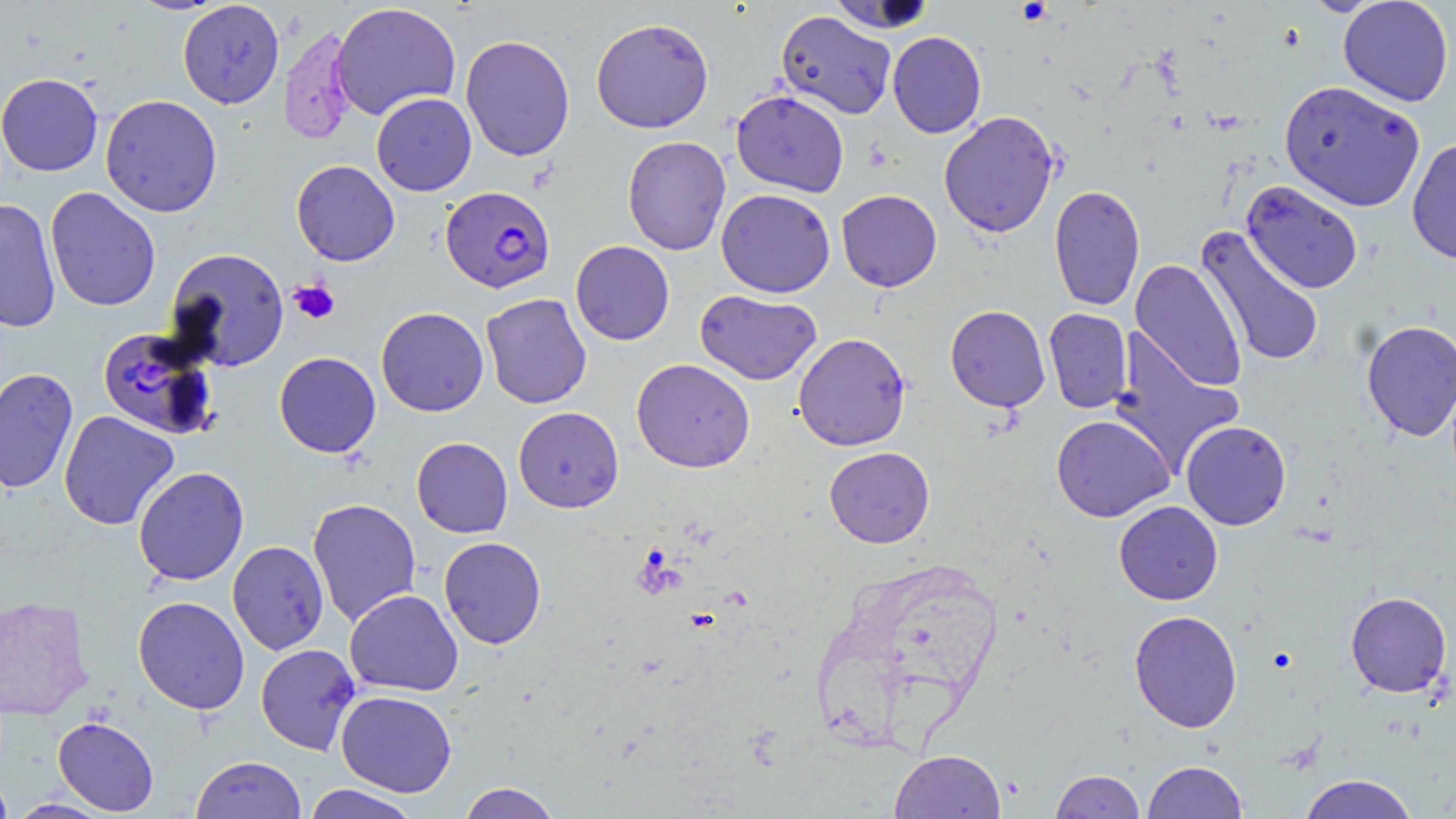

Summary:
  - Coordinate format: approximate bounding boxes as (x1,y1)-(x2,y2) corner pairs in pixels
  - Platelet locations: (289,280)-(340,324)
  - Uninfected red blood cell locations: (1338,0)-(1454,106), (178,1)-(284,108), (825,1)-(938,34), (330,2)-(461,120), (775,10)-(896,120), (590,18)-(714,133), (279,24)-(358,145), (887,31)-(987,138), (460,34)-(576,162), (0,73)-(103,176), (1279,80)-(1425,212), (731,90)-(849,197), (371,93)-(476,196), (100,95)-(223,217), (938,111)-(1060,238), (622,135)-(731,256), (1407,138)-(1456,266), (291,160)-(400,266), (1241,180)-(1364,295), (1048,185)-(1145,311), (45,187)-(160,312), (716,188)-(835,298), (836,189)-(942,292), (0,199)-(62,333), (1195,227)-(1325,368), (570,241)-(675,345), (164,248)-(290,372), (1130,259)-(1246,391), (695,289)-(822,385), (480,293)-(592,409), (945,305)-(1050,412), (376,307)-(489,416), (1043,308)-(1133,413), (1361,320)-(1456,442), (1109,330)-(1244,475), (793,333)-(911,451), (274,352)-(381,457), (631,358)-(756,473), (0,367)-(79,494), (513,407)-(624,513), (59,411)-(179,531), (1051,415)-(1175,522), (1181,420)-(1291,530), (411,437)-(513,538), (823,446)-(935,548), (133,466)-(249,586), (307,498)-(421,626), (1114,500)-(1223,605), (439,537)-(547,649), (227,540)-(329,655), (344,589)-(464,696), (1345,591)-(1452,697), (0,596)-(93,719), (133,596)-(250,715), (1129,610)-(1243,733), (255,644)-(361,755), (335,690)-(457,797), (53,716)-(159,815), (889,749)-(1006,819), (190,756)-(306,818), (1141,760)-(1248,819), (1049,769)-(1145,818), (0,772)-(14,819), (1297,774)-(1420,819), (457,782)-(563,819), (302,784)-(422,819), (7,799)-(113,818)
  - Plasmodium falciparum-infected red blood cell locations: (441,186)-(556,293), (96,326)-(220,440)
  - Slide-level diagnosis: Plasmodium falciparum
  - Preparation: thin blood smear
  - Field of view: single
  - Stain: May-Grünwald-Giemsa
  - Image size: 1456×819 pixels
  - Magnification: 1000x
  - Modality: light microscopy